Report the malaria status of this cell.
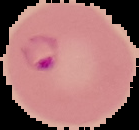

Parasitized.

Summary:
  - Image type: segmented cell region on a black background
  - Preparation: thin blood film
  - Image size: 139×130 pixels